Report the malaria status of this cell.
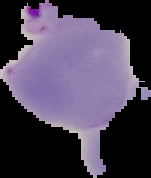

Parasitized.

Summary:
  - Image type: segmented cell region on a black background
  - Preparation: thin blood smear
  - Image size: 151×178 pixels